State which parasite is depicted.
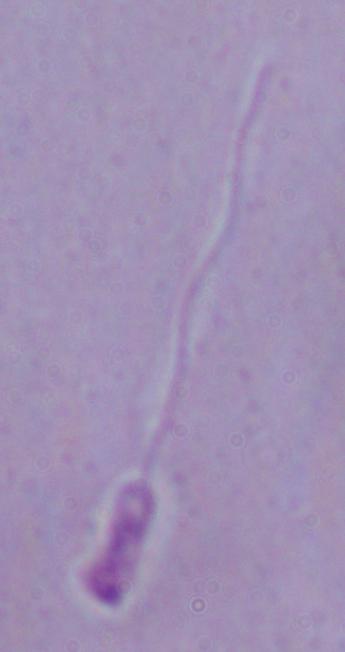
Leishmania.

Summary:
  - Magnification: 1000x
  - Modality: micrograph